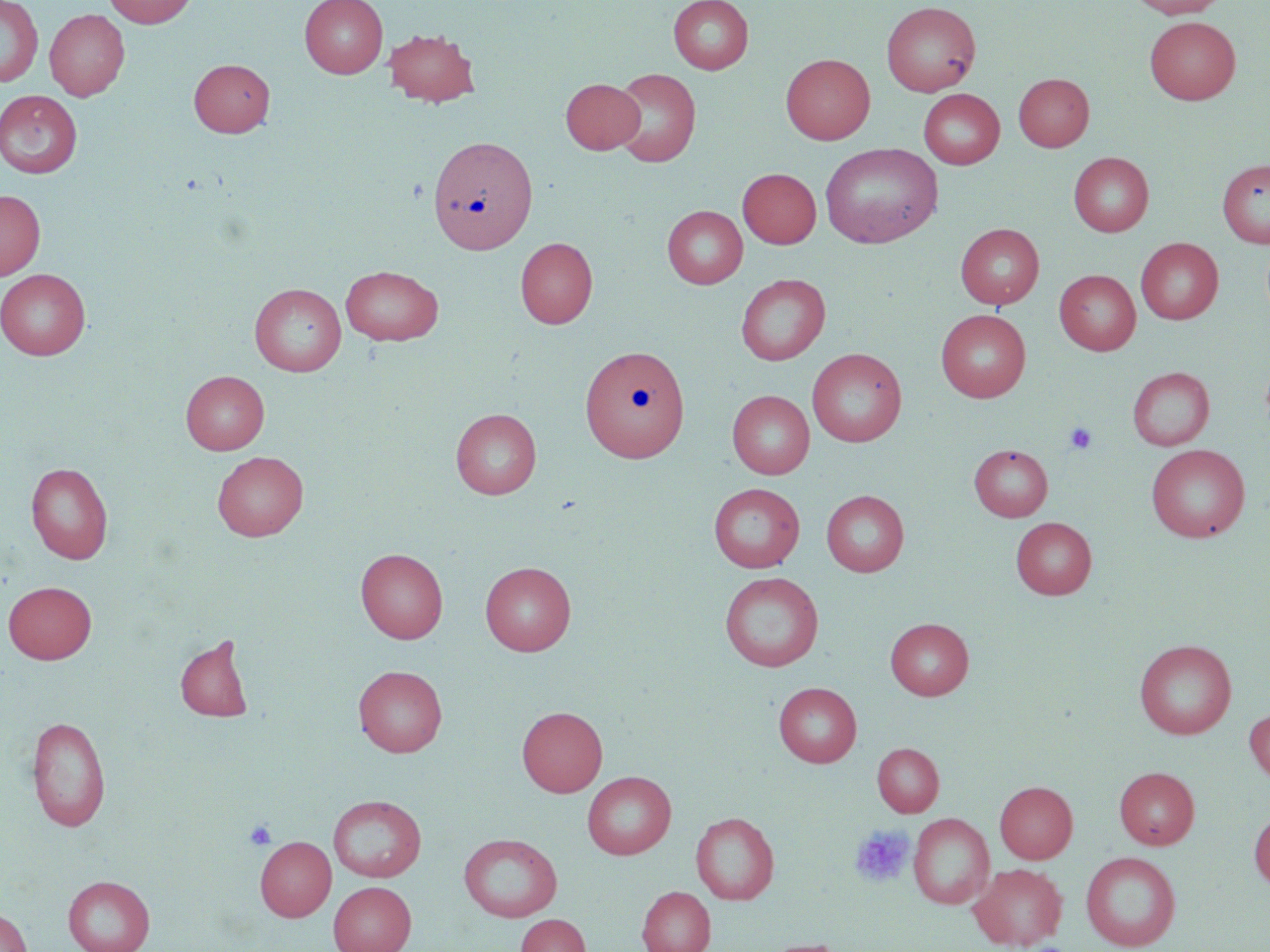

slide_level_diagnosis: no evidence of blood parasites
magnification: 1000x
modality: optical microscopy
uninfected_red_blood_cell_locations: 'approximate bounding boxes as (x1,y1)-(x2,y2) corner pairs in pixels: (104,0)-(197,28), (300,0)-(388,78), (668,0)-(753,74), (1128,0)-(1229,18), (0,1)-(43,87), (881,1)-(981,97), (44,9)-(130,101), (1144,16)-(1241,104), (383,28)-(480,107), (781,53)-(875,144), (189,58)-(275,137), (608,67)-(701,167), (1013,73)-(1094,151), (561,78)-(645,154), (918,89)-(1005,169), (0,90)-(83,178), (428,135)-(538,254), (820,142)-(942,247), (1068,152)-(1154,237), (1217,159)-(1270,248), (738,168)-(821,248), (0,190)-(45,279), (662,205)-(747,288), (956,223)-(1044,309), (515,237)-(598,328), (1136,237)-(1223,324), (341,265)-(443,345), (0,269)-(91,360), (1054,269)-(1141,355), (736,274)-(830,365), (249,283)-(346,376), (936,310)-(1031,401), (580,345)-(690,462), (807,348)-(906,446), (1127,366)-(1215,450), (181,370)-(269,454), (727,390)-(815,479), (450,408)-(541,499), (968,444)-(1053,521), (1146,444)-(1250,542), (212,451)-(308,541), (26,462)-(113,563), (708,482)-(805,572), (821,489)-(909,577), (1010,517)-(1096,599), (356,547)-(448,643), (480,561)-(576,656), (719,571)-(824,671), (3,580)-(96,663), (885,618)-(973,699), (175,633)-(255,722), (1134,640)-(1236,739), (354,665)-(447,756), (773,682)-(862,767), (517,705)-(607,797), (1245,707)-(1270,786), (27,715)-(110,832), (872,743)-(944,817), (1114,766)-(1200,849), (582,771)-(676,859), (995,781)-(1077,863), (328,794)-(426,882), (1249,808)-(1270,891), (691,811)-(779,904), (909,813)-(994,910), (458,833)-(563,922), (255,836)-(336,921), (1081,851)-(1181,951), (969,862)-(1067,950), (63,875)-(155,952), (328,880)-(416,952), (637,886)-(715,952), (0,908)-(32,952), (516,914)-(590,952)'
preparation: thin blood film
stain: May-Grünwald-Giemsa
platelet_locations: 'approximate bounding boxes as (x1,y1)-(x2,y2) corner pairs in pixels: (1065,423)-(1098,454), (244,820)-(277,850), (850,825)-(914,888)'
field_of_view: single
image_size: 1270×952 pixels